Report the malaria status of this cell.
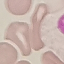

It is uninfected.

Thin blood smear. Giemsa-stained preparation. Cell patch, automatically extracted from a larger field of view and resized to 64 × 64 pixels. Photographed with a smartphone camera at the microscope eyepiece.